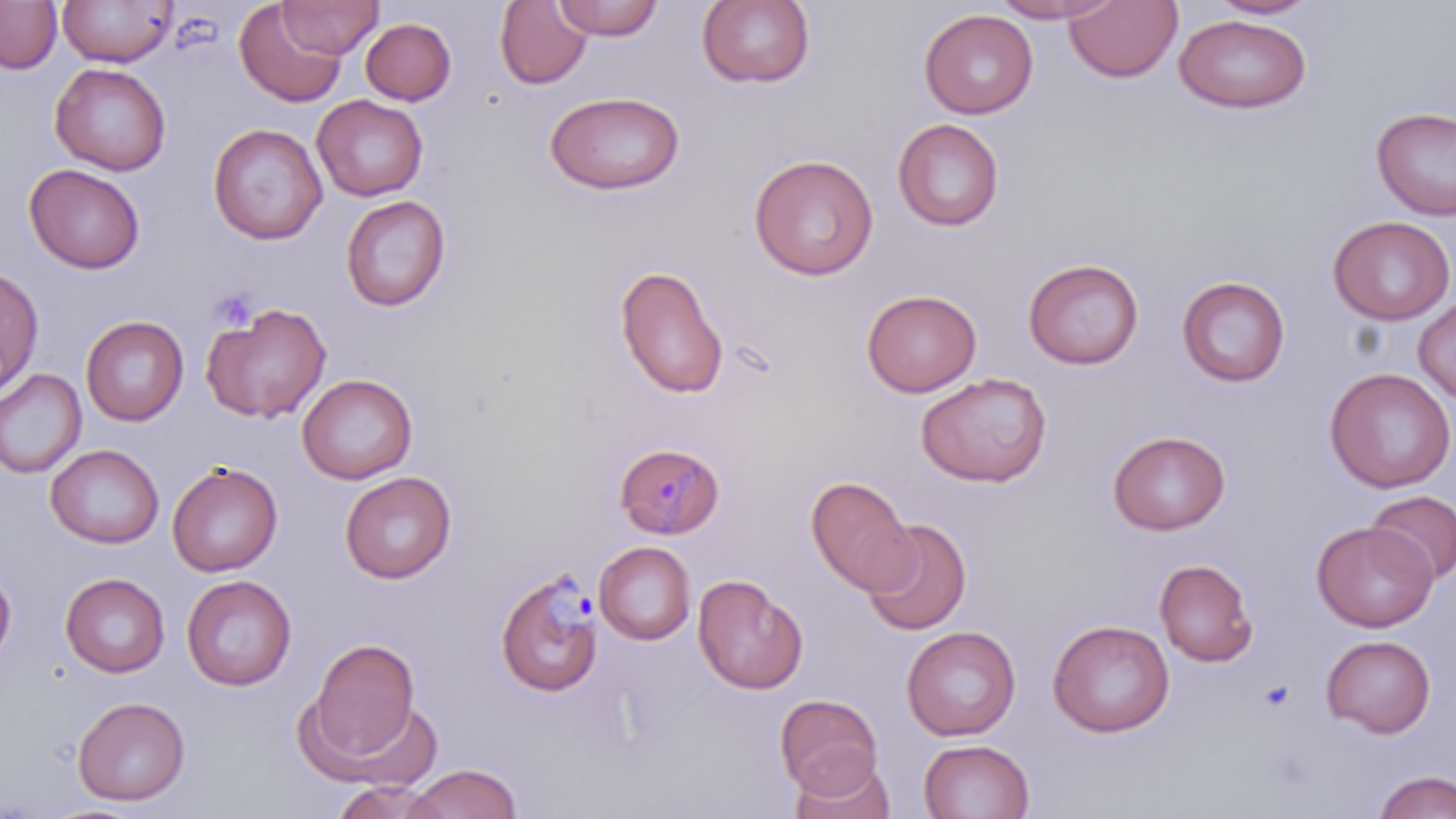

slide_level_diagnosis: Plasmodium malariae
stain: May-Grünwald-Giemsa
uninfected_red_blood_cell_locations: 'approximate bounding boxes as (x1,y1)-(x2,y2) corner pairs in pixels: (0,0)-(62,74), (57,0)-(178,67), (278,0)-(383,58), (553,0)-(663,40), (989,0)-(1123,23), (1206,0)-(1319,20), (234,1)-(348,108), (495,1)-(592,89), (696,1)-(816,89), (1065,1)-(1182,83), (919,8)-(1038,119), (1174,14)-(1311,113), (360,18)-(456,105), (50,63)-(171,175), (544,90)-(686,195), (312,95)-(428,201), (1371,106)-(1456,220), (893,118)-(1004,231), (208,123)-(327,245), (748,153)-(879,281), (24,164)-(145,274), (340,195)-(451,311), (1328,215)-(1455,325), (1023,258)-(1144,370), (614,264)-(729,399), (0,265)-(43,397), (1176,276)-(1290,387), (862,289)-(982,397), (1414,296)-(1456,404), (200,302)-(332,424), (81,315)-(189,426), (0,368)-(87,479), (1324,368)-(1456,493), (915,372)-(1053,487), (297,373)-(417,484), (1108,430)-(1231,535), (46,444)-(164,548), (167,461)-(283,576), (339,471)-(456,583), (805,475)-(916,594), (1366,491)-(1455,585), (861,517)-(972,636), (1311,521)-(1437,631), (593,541)-(696,645), (1154,558)-(1258,667), (0,564)-(16,668), (60,572)-(170,677), (181,574)-(297,691), (693,574)-(807,694), (1048,619)-(1174,738), (901,625)-(1020,741), (1321,634)-(1435,738), (305,637)-(422,766), (774,694)-(884,798), (72,696)-(190,806), (918,738)-(1035,819), (789,757)-(896,819), (407,763)-(521,819), (1372,770)-(1456,819), (331,779)-(449,819)'
image_size: 1456×819 pixels
magnification: 1000x
modality: optical microscopy
plasmodium_malariae_infected_red_blood_cell_locations: 'approximate bounding boxes as (x1,y1)-(x2,y2) corner pairs in pixels: (614,442)-(725,539), (496,568)-(604,698)'
preparation: thin blood smear
platelet_locations: 'approximate bounding boxes as (x1,y1)-(x2,y2) corner pairs in pixels: (210,288)-(258,333)'
field_of_view: one of a larger specimen